Assess this cell for malaria.
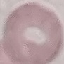
Uninfected.

capture = smartphone camera at the microscope eyepiece
image type = automatically extracted cell patch, resized to 64 × 64 pixels
preparation = thin blood smear
stain = Giemsa